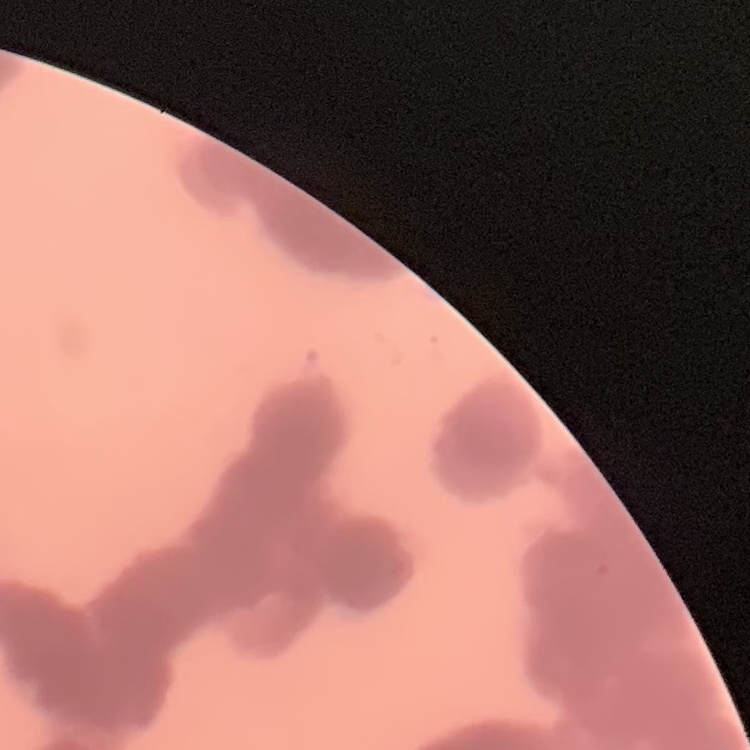

erythrocyte_morphology: rouleaux formation
image_type: square crop of a larger photomicrograph
preparation: thin blood smear
stain: Field's or Giemsa